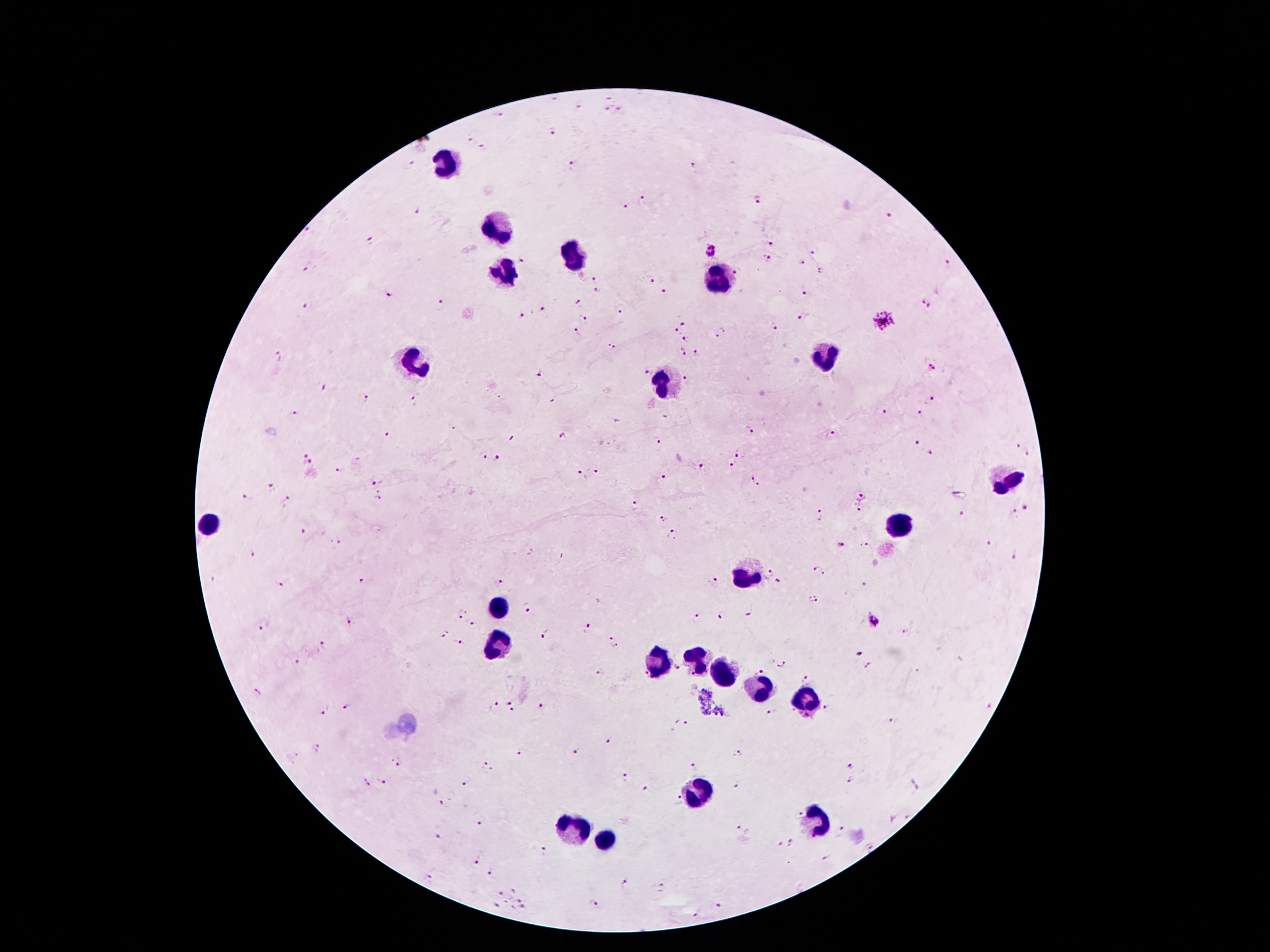 Approximate centers as {x, y} in pixels. Leukocyte locations: {446, 162}, {496, 230}, {573, 256}, {504, 273}, {715, 281}, {823, 352}, {416, 362}, {665, 382}, {1006, 482}, {895, 523}, {211, 525}, {741, 575}, {500, 606}, {497, 647}, {695, 660}, {657, 664}, {721, 676}, {761, 692}, {805, 701}, {701, 791}, {812, 822}, {573, 827}, {603, 840}. Plasmodium parasite locations (subset; some too small to resolve): {608, 95}, {552, 98}, {579, 106}, {620, 108}, {607, 109}, {499, 115}, {555, 133}, {471, 139}, {483, 147}, {411, 165}, {692, 166}, {573, 167}, {643, 197}, {758, 199}, {627, 207}, {417, 211}, {889, 217}, {308, 230}, {369, 240}, {770, 243}, {711, 252}, {813, 253}, {768, 259}, {523, 260}, {802, 261}, {946, 262}, {307, 268}, {736, 272}, {822, 272}, {594, 280}, {651, 282}, {597, 291}, {389, 292}, {665, 292}, {805, 292}, {579, 304}, {926, 304}, {441, 305}, {308, 307}, {542, 311}, {621, 312}, {522, 315}, {804, 316}, {586, 319}, {883, 321}, {684, 322}, {774, 327}, {676, 330}, {578, 332}, {720, 333}, {686, 338}, {612, 346}, {682, 352}, {696, 353}, {277, 356}, {931, 368}, {539, 373}, {645, 373}, {688, 378}, {323, 385}, {364, 398}, {934, 399}, {414, 401}, {885, 412}, {294, 413}, {920, 415}, {749, 430}, {387, 434}, {832, 435}, {563, 436}, {657, 440}, {918, 443}, {1016, 445}, {929, 450}, {1027, 451}, {483, 455}, {739, 455}, {497, 457}, {308, 459}, {732, 465}, {701, 467}, {339, 471}, {597, 472}, {580, 473}, {665, 477}, {752, 478}, {373, 483}, {273, 486}, {758, 487}, {378, 496}, {862, 496}, {246, 497}, {288, 499}, {635, 505}, {1024, 508}, {860, 510}, {1013, 512}, {963, 513}, {819, 515}, {663, 519}, {303, 530}, {672, 534}, {338, 542}, {840, 544}, {865, 544}, {990, 544}, {253, 553}, {1014, 555}, {819, 571}, {773, 572}, {361, 581}, {715, 581}, {500, 583}, {778, 583}, {281, 586}, {813, 600}, {526, 607}, {460, 613}, {720, 614}, {750, 614}, {699, 615}, {351, 620}, {874, 622}, {472, 623}, {262, 625}, {587, 627}, {905, 630}, {445, 635}, {546, 635}, {613, 641}, {460, 643}, {326, 645}, {859, 654}, {298, 662}, {780, 662}, {867, 664}, {677, 670}, {761, 670}, {600, 671}, {644, 674}, {808, 679}, {258, 692}, {509, 703}, {495, 706}, {541, 706}, {827, 706}, {348, 707}, {324, 710}, {514, 710}, {771, 711}, {892, 721}, {677, 723}, {686, 725}, {609, 741}, {318, 749}, {519, 752}, {576, 752}, {737, 754}, {398, 762}, {851, 765}, {487, 766}, {694, 768}, {625, 777}, {466, 781}, {850, 781}, {381, 782}, {366, 784}, {738, 786}, {645, 788}, {679, 801}, {443, 803}, {800, 812}, {480, 823}, {739, 827}, {842, 829}, {437, 835}, {780, 843}, {789, 843}, {872, 847}, {544, 849}, {825, 857}, {476, 861}, {490, 873}, {430, 876}, {626, 881}, {662, 886}, {515, 890}, {499, 894}, {521, 899}, {596, 902}, {497, 905}, {721, 905}, {523, 908}, {696, 916}. One field from this slide. Thick blood smear. Giemsa stain. Image is 1270×952 pixels. Patient malaria status: infected with Plasmodium falciparum. Smartphone photograph taken through the microscope eyepiece. 100x magnification.